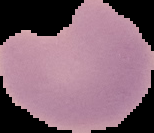

Summary:
  - Image size: 154×133 pixels
  - Malaria status: uninfected
  - Preparation: thin blood film
  - Image type: segmented cell region with the area outside set to black